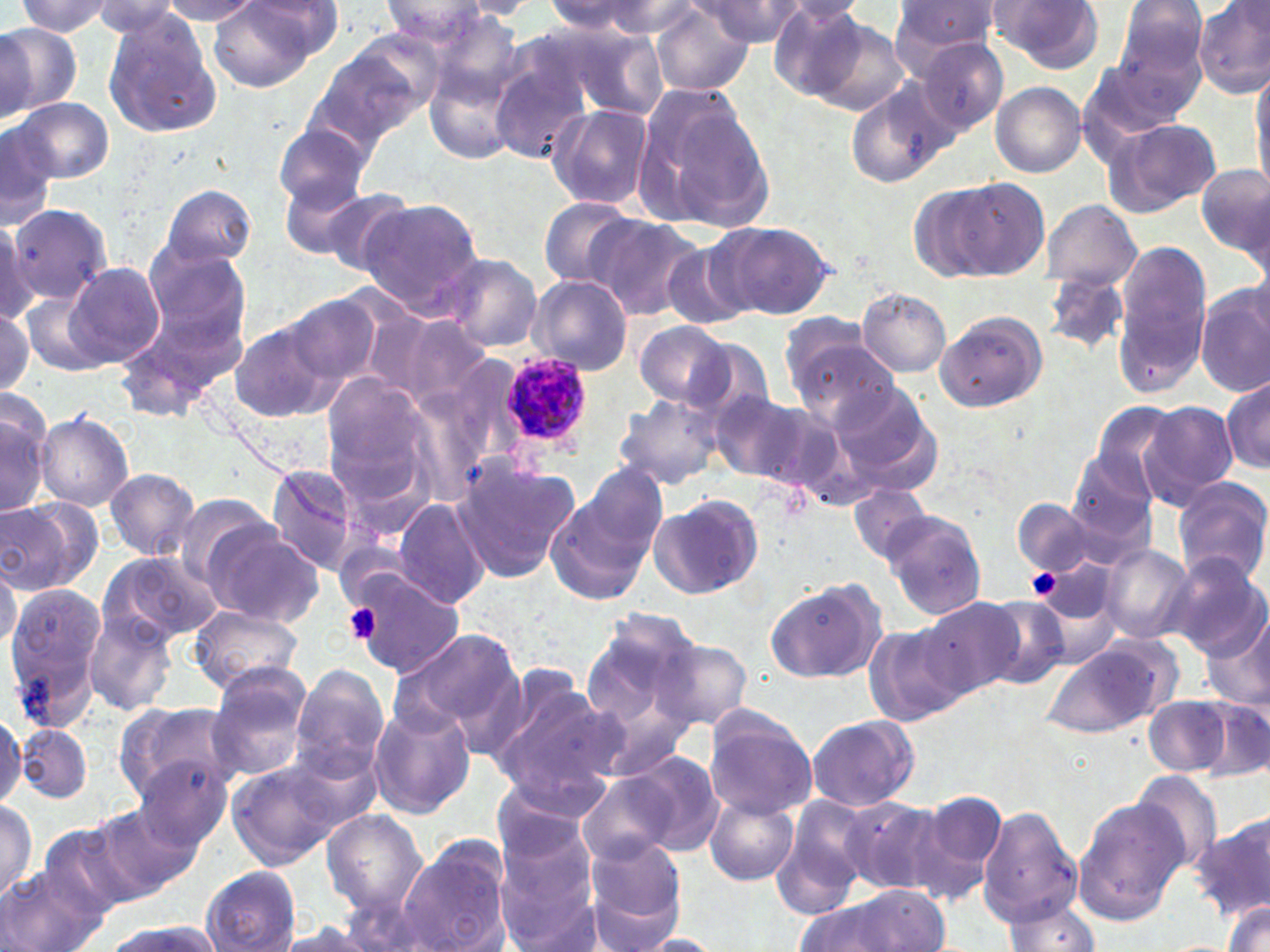

slide-level diagnosis = Plasmodium ovale
field of view = one of a larger specimen
preparation = thin blood smear
image size = 1270×952 pixels
modality = optical microscopy
stain = May-Grünwald-Giemsa
platelet locations = approximate bounding boxes as named x1/y1/x2/y2 corners in pixels: (x1=1025, y1=567, x2=1061, y2=599), (x1=342, y1=603, x2=381, y2=645)
uninfected red blood cell locations = approximate bounding boxes as named x1/y1/x2/y2 corners in pixels: (x1=246, y1=0, x2=346, y2=58), (x1=697, y1=0, x2=807, y2=46), (x1=987, y1=0, x2=1103, y2=70), (x1=1115, y1=0, x2=1209, y2=91), (x1=15, y1=1, x2=120, y2=37), (x1=158, y1=1, x2=267, y2=24), (x1=208, y1=1, x2=331, y2=89), (x1=380, y1=1, x2=489, y2=44), (x1=455, y1=1, x2=541, y2=18), (x1=774, y1=1, x2=869, y2=26), (x1=887, y1=1, x2=1003, y2=70), (x1=1194, y1=1, x2=1270, y2=99), (x1=88, y1=2, x2=186, y2=37), (x1=540, y1=2, x2=662, y2=38), (x1=769, y1=3, x2=870, y2=101), (x1=651, y1=5, x2=754, y2=96), (x1=101, y1=12, x2=223, y2=140), (x1=806, y1=16, x2=909, y2=115), (x1=0, y1=23, x2=77, y2=121), (x1=0, y1=24, x2=37, y2=120), (x1=558, y1=24, x2=668, y2=119), (x1=308, y1=39, x2=437, y2=149), (x1=916, y1=39, x2=1009, y2=136), (x1=487, y1=52, x2=593, y2=168), (x1=423, y1=53, x2=525, y2=170), (x1=1077, y1=59, x2=1190, y2=156), (x1=1250, y1=70, x2=1270, y2=193), (x1=845, y1=79, x2=956, y2=190), (x1=991, y1=82, x2=1086, y2=178), (x1=633, y1=86, x2=775, y2=233), (x1=9, y1=96, x2=115, y2=183), (x1=545, y1=103, x2=656, y2=209), (x1=1103, y1=118, x2=1222, y2=218), (x1=0, y1=121, x2=57, y2=227), (x1=275, y1=125, x2=373, y2=212), (x1=1196, y1=161, x2=1269, y2=262), (x1=278, y1=176, x2=379, y2=263), (x1=952, y1=179, x2=1049, y2=279), (x1=908, y1=184, x2=1005, y2=281), (x1=159, y1=185, x2=256, y2=270), (x1=309, y1=185, x2=418, y2=276), (x1=357, y1=196, x2=483, y2=315), (x1=537, y1=196, x2=641, y2=287), (x1=1038, y1=199, x2=1142, y2=291), (x1=3, y1=202, x2=111, y2=307), (x1=587, y1=215, x2=705, y2=320), (x1=718, y1=221, x2=833, y2=320), (x1=661, y1=240, x2=754, y2=332), (x1=140, y1=244, x2=251, y2=350), (x1=1112, y1=245, x2=1211, y2=394), (x1=442, y1=253, x2=543, y2=352), (x1=63, y1=261, x2=164, y2=367), (x1=1041, y1=271, x2=1130, y2=357), (x1=526, y1=274, x2=633, y2=377), (x1=21, y1=286, x2=116, y2=378), (x1=857, y1=289, x2=951, y2=376), (x1=1196, y1=289, x2=1269, y2=398), (x1=276, y1=293, x2=385, y2=392), (x1=0, y1=308, x2=35, y2=398), (x1=933, y1=308, x2=1047, y2=412), (x1=379, y1=311, x2=491, y2=410), (x1=779, y1=316, x2=883, y2=403), (x1=229, y1=321, x2=339, y2=423), (x1=634, y1=321, x2=733, y2=409), (x1=114, y1=323, x2=217, y2=418), (x1=793, y1=338, x2=899, y2=431), (x1=321, y1=372, x2=435, y2=499), (x1=1222, y1=374, x2=1269, y2=475), (x1=832, y1=383, x2=933, y2=478), (x1=709, y1=387, x2=816, y2=486), (x1=614, y1=390, x2=725, y2=490), (x1=0, y1=393, x2=53, y2=519), (x1=1092, y1=402, x2=1179, y2=498), (x1=1139, y1=402, x2=1239, y2=507), (x1=34, y1=413, x2=134, y2=512), (x1=1068, y1=449, x2=1159, y2=546), (x1=450, y1=458, x2=579, y2=582), (x1=263, y1=461, x2=365, y2=577), (x1=580, y1=464, x2=667, y2=559), (x1=104, y1=467, x2=200, y2=560), (x1=1172, y1=476, x2=1270, y2=587), (x1=850, y1=484, x2=933, y2=564), (x1=544, y1=488, x2=655, y2=609), (x1=647, y1=493, x2=764, y2=600), (x1=391, y1=496, x2=490, y2=609), (x1=0, y1=497, x2=98, y2=594), (x1=1011, y1=499, x2=1112, y2=578), (x1=879, y1=508, x2=987, y2=620), (x1=200, y1=525, x2=325, y2=628), (x1=1100, y1=544, x2=1194, y2=645), (x1=100, y1=550, x2=223, y2=645), (x1=1164, y1=553, x2=1269, y2=658), (x1=1033, y1=560, x2=1121, y2=653), (x1=0, y1=562, x2=21, y2=651), (x1=347, y1=571, x2=464, y2=676), (x1=764, y1=577, x2=889, y2=685), (x1=2, y1=587, x2=105, y2=727), (x1=979, y1=595, x2=1073, y2=689), (x1=917, y1=597, x2=1022, y2=698), (x1=189, y1=604, x2=303, y2=693), (x1=85, y1=608, x2=179, y2=716), (x1=578, y1=609, x2=704, y2=752), (x1=1199, y1=613, x2=1270, y2=713), (x1=863, y1=623, x2=969, y2=727), (x1=394, y1=627, x2=523, y2=735), (x1=652, y1=637, x2=753, y2=731), (x1=1042, y1=643, x2=1164, y2=738), (x1=206, y1=663, x2=314, y2=780), (x1=290, y1=665, x2=389, y2=781), (x1=489, y1=676, x2=622, y2=809), (x1=1142, y1=694, x2=1238, y2=778), (x1=1190, y1=694, x2=1269, y2=783), (x1=114, y1=699, x2=235, y2=802), (x1=366, y1=702, x2=476, y2=820), (x1=702, y1=708, x2=818, y2=819), (x1=0, y1=711, x2=25, y2=812), (x1=805, y1=715, x2=922, y2=812), (x1=16, y1=724, x2=92, y2=803), (x1=627, y1=749, x2=726, y2=856), (x1=132, y1=757, x2=230, y2=854), (x1=225, y1=758, x2=354, y2=869), (x1=577, y1=771, x2=676, y2=865), (x1=1130, y1=771, x2=1225, y2=875), (x1=913, y1=790, x2=1010, y2=906), (x1=704, y1=793, x2=800, y2=886), (x1=771, y1=795, x2=870, y2=919), (x1=841, y1=795, x2=949, y2=896), (x1=0, y1=798, x2=39, y2=899), (x1=1071, y1=798, x2=1185, y2=926), (x1=90, y1=806, x2=197, y2=899), (x1=976, y1=807, x2=1082, y2=922), (x1=323, y1=811, x2=427, y2=911), (x1=1193, y1=813, x2=1270, y2=921), (x1=494, y1=818, x2=604, y2=949), (x1=31, y1=819, x2=140, y2=927), (x1=400, y1=836, x2=511, y2=952), (x1=580, y1=838, x2=687, y2=950), (x1=2, y1=865, x2=108, y2=952), (x1=203, y1=867, x2=301, y2=951), (x1=806, y1=887, x2=955, y2=952), (x1=1222, y1=899, x2=1270, y2=952), (x1=998, y1=900, x2=1104, y2=951), (x1=268, y1=921, x2=393, y2=952), (x1=104, y1=922, x2=219, y2=952), (x1=633, y1=934, x2=727, y2=950)
Plasmodium ovale-infected red blood cell locations = approximate bounding boxes as named x1/y1/x2/y2 corners in pixels: (x1=500, y1=352, x2=594, y2=445)
magnification = 1000x